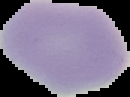

Summary:
  - Image type: cell region segmented out of the field of view; surrounding area masked to black
  - Image size: 130×97 pixels
  - Result: no Plasmodium parasites seen
  - Preparation: thin blood film